Locate and identify every blood parasite.
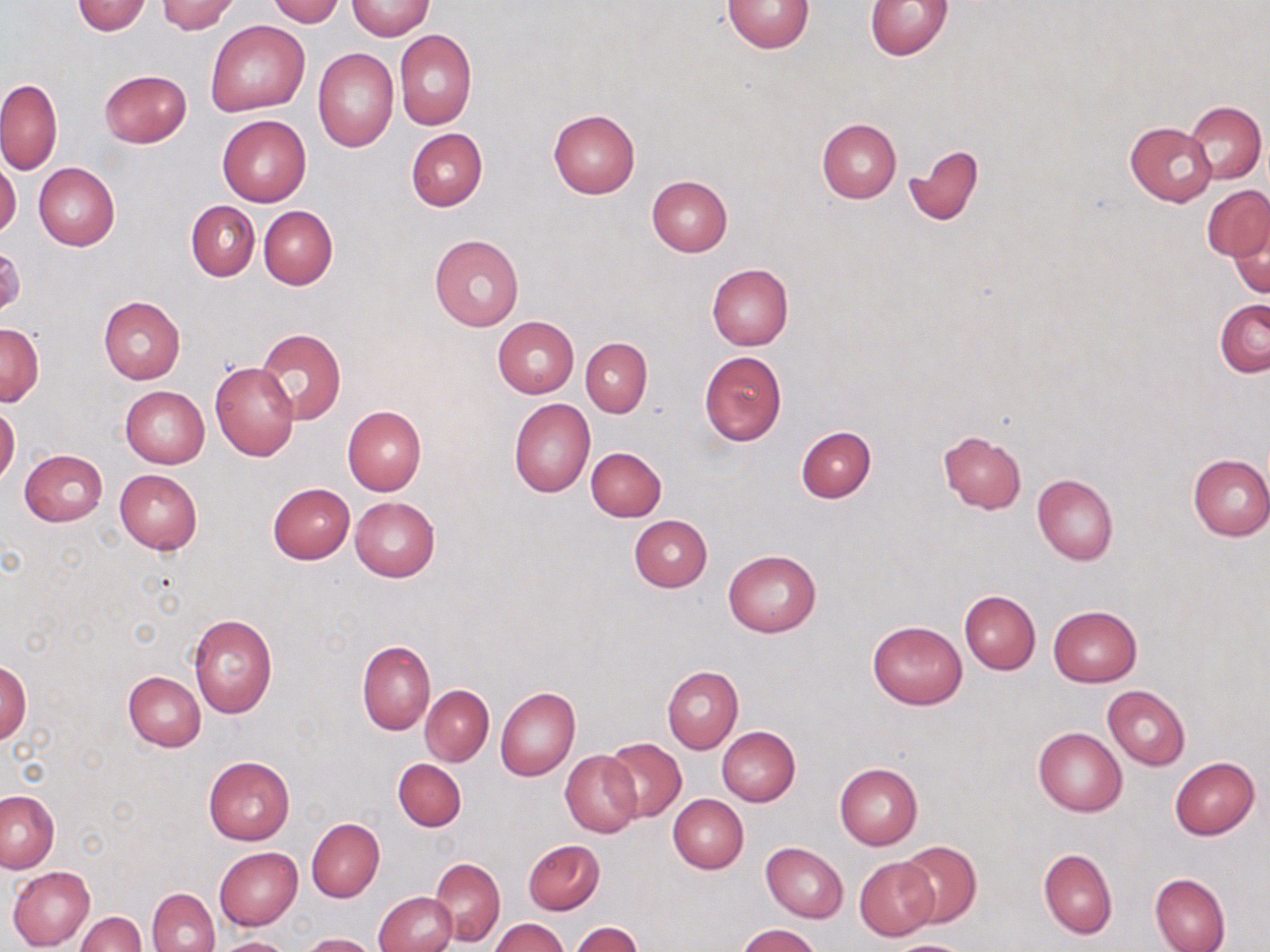

No blood parasites observed.

slide-level diagnosis = negative for blood parasites
magnification = 1000x
stain = May-Grünwald-Giemsa
preparation = thin blood film
field of view = one of a larger specimen
modality = optical microscopy
image size = 1270×952 pixels
uninfected red blood cell locations = approximate bounding boxes as named x1/y1/x2/y2 corners in pixels: (x1=155, y1=0, x2=241, y2=33), (x1=267, y1=0, x2=343, y2=26), (x1=70, y1=1, x2=153, y2=35), (x1=347, y1=1, x2=434, y2=40), (x1=722, y1=1, x2=815, y2=52), (x1=865, y1=1, x2=953, y2=59), (x1=206, y1=20, x2=310, y2=116), (x1=394, y1=29, x2=477, y2=131), (x1=313, y1=48, x2=398, y2=152), (x1=100, y1=69, x2=192, y2=147), (x1=0, y1=79, x2=62, y2=173), (x1=1186, y1=101, x2=1266, y2=183), (x1=547, y1=109, x2=640, y2=198), (x1=218, y1=114, x2=311, y2=206), (x1=817, y1=119, x2=900, y2=203), (x1=1124, y1=121, x2=1217, y2=206), (x1=406, y1=128, x2=487, y2=211), (x1=903, y1=144, x2=984, y2=227), (x1=0, y1=161, x2=21, y2=240), (x1=33, y1=163, x2=120, y2=250), (x1=645, y1=175, x2=732, y2=256), (x1=1203, y1=186, x2=1270, y2=261), (x1=186, y1=201, x2=259, y2=281), (x1=258, y1=206, x2=336, y2=289), (x1=1229, y1=214, x2=1269, y2=299), (x1=429, y1=234, x2=524, y2=331), (x1=706, y1=264, x2=793, y2=350), (x1=97, y1=296, x2=186, y2=383), (x1=1214, y1=299, x2=1269, y2=378), (x1=493, y1=316, x2=579, y2=398), (x1=0, y1=322, x2=43, y2=405), (x1=255, y1=330, x2=347, y2=425), (x1=580, y1=338, x2=651, y2=416), (x1=700, y1=351, x2=787, y2=445), (x1=211, y1=364, x2=298, y2=461), (x1=120, y1=385, x2=209, y2=468), (x1=509, y1=398, x2=594, y2=497), (x1=0, y1=404, x2=20, y2=484), (x1=343, y1=405, x2=426, y2=495), (x1=796, y1=427, x2=875, y2=502), (x1=937, y1=432, x2=1025, y2=513), (x1=585, y1=446, x2=666, y2=520), (x1=20, y1=449, x2=107, y2=527), (x1=1186, y1=452, x2=1270, y2=541), (x1=115, y1=469, x2=202, y2=555), (x1=1032, y1=473, x2=1118, y2=565), (x1=268, y1=483, x2=355, y2=564), (x1=350, y1=496, x2=440, y2=581), (x1=629, y1=514, x2=712, y2=592), (x1=723, y1=549, x2=822, y2=637), (x1=959, y1=590, x2=1041, y2=674), (x1=1048, y1=605, x2=1143, y2=687), (x1=189, y1=614, x2=277, y2=718), (x1=867, y1=620, x2=968, y2=708), (x1=357, y1=640, x2=435, y2=734), (x1=1, y1=661, x2=31, y2=744), (x1=663, y1=666, x2=743, y2=753), (x1=123, y1=671, x2=206, y2=750), (x1=495, y1=685, x2=579, y2=781), (x1=1103, y1=685, x2=1190, y2=769), (x1=420, y1=686, x2=493, y2=765), (x1=717, y1=726, x2=800, y2=806), (x1=1033, y1=727, x2=1126, y2=816), (x1=603, y1=738, x2=686, y2=822), (x1=560, y1=749, x2=643, y2=838), (x1=203, y1=754, x2=296, y2=845), (x1=1169, y1=756, x2=1260, y2=840), (x1=393, y1=758, x2=466, y2=830), (x1=834, y1=762, x2=922, y2=849), (x1=0, y1=790, x2=59, y2=873), (x1=668, y1=793, x2=749, y2=873), (x1=307, y1=819, x2=384, y2=902), (x1=524, y1=839, x2=604, y2=915), (x1=895, y1=840, x2=981, y2=927), (x1=761, y1=842, x2=849, y2=922), (x1=215, y1=846, x2=302, y2=929), (x1=1038, y1=847, x2=1116, y2=939), (x1=429, y1=857, x2=504, y2=946), (x1=854, y1=857, x2=938, y2=939), (x1=8, y1=866, x2=94, y2=950), (x1=1149, y1=873, x2=1231, y2=952), (x1=147, y1=887, x2=219, y2=952), (x1=374, y1=891, x2=456, y2=952), (x1=75, y1=912, x2=146, y2=951), (x1=489, y1=918, x2=570, y2=952), (x1=570, y1=922, x2=643, y2=952), (x1=737, y1=924, x2=821, y2=952), (x1=300, y1=933, x2=378, y2=952), (x1=212, y1=936, x2=295, y2=952)
platelet locations = approximate bounding boxes as named x1/y1/x2/y2 corners in pixels: (x1=0, y1=248, x2=26, y2=316)